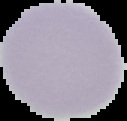

malaria status = uninfected
image type = segmented cell region on a black background
image size = 127×121 pixels
preparation = thin blood smear